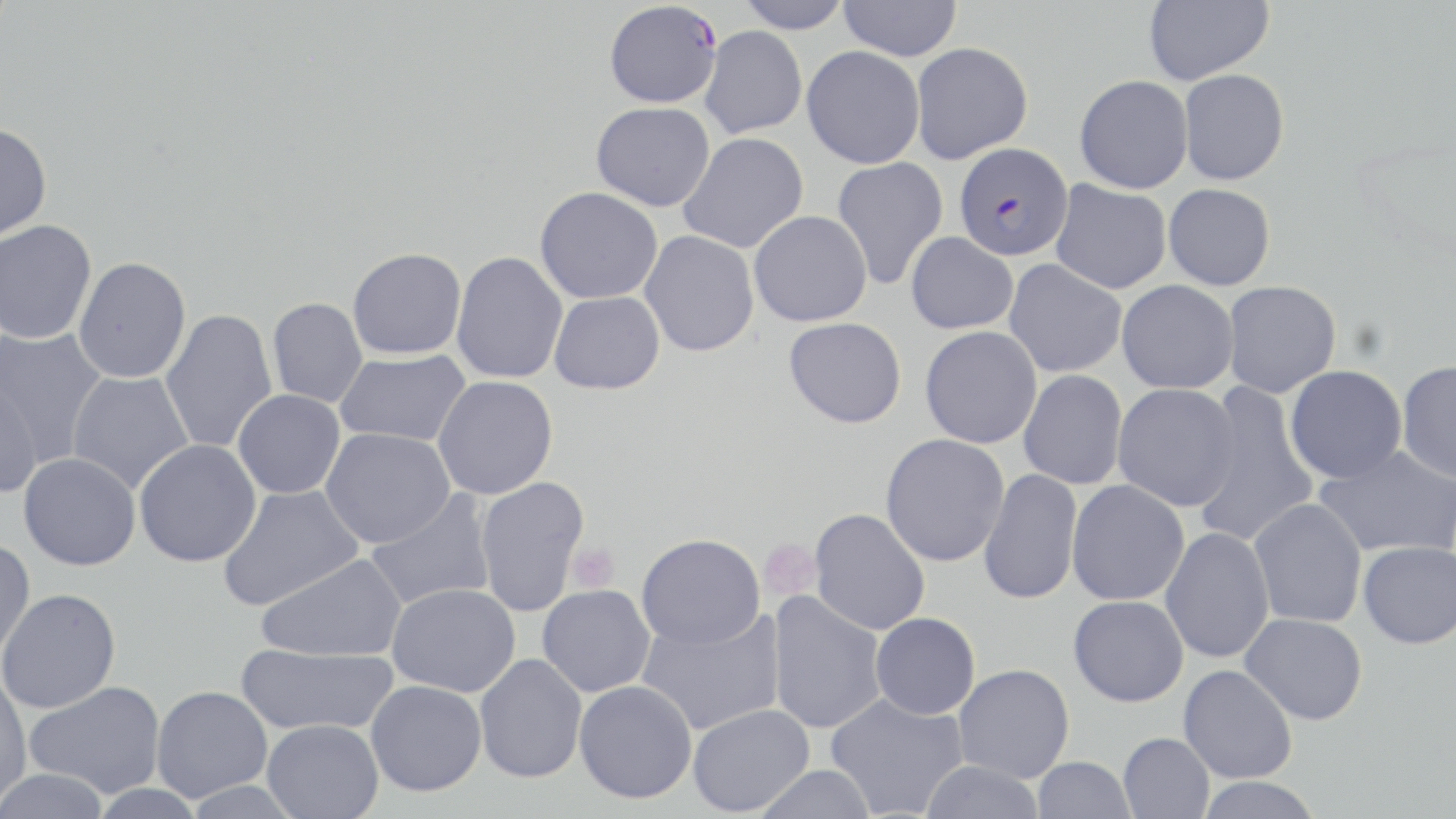

Summary:
  - Coordinate format: approximate bounding boxes as (x1, y1, x2, y2) in pixels
  - Plasmodium falciparum-infected red blood cell locations: (604, 1, 722, 108), (954, 142, 1074, 261)
  - Uninfected red blood cell locations: (734, 0, 853, 33), (838, 0, 962, 61), (1142, 0, 1273, 85), (700, 25, 807, 138), (910, 42, 1033, 164), (801, 46, 925, 168), (1178, 69, 1290, 186), (1074, 74, 1193, 194), (590, 101, 715, 212), (0, 122, 52, 242), (678, 132, 809, 254), (832, 158, 948, 290), (1051, 179, 1172, 294), (1163, 183, 1275, 291), (535, 187, 663, 304), (749, 210, 872, 327), (0, 219, 97, 345), (640, 230, 760, 357), (906, 232, 1018, 335), (347, 247, 466, 360), (451, 251, 568, 384), (73, 256, 192, 383), (1004, 259, 1127, 378), (1116, 280, 1239, 393), (1222, 280, 1341, 399), (549, 291, 665, 394), (267, 298, 367, 408), (159, 308, 278, 454), (784, 317, 907, 428), (920, 325, 1042, 449), (0, 326, 108, 469), (334, 350, 471, 447), (1397, 360, 1456, 484), (1284, 365, 1408, 484), (1018, 369, 1128, 490), (66, 370, 194, 494), (0, 375, 43, 499), (433, 375, 558, 499), (1191, 382, 1320, 549), (1112, 383, 1241, 511), (232, 389, 346, 499), (320, 427, 456, 548), (880, 433, 1010, 567), (134, 439, 262, 567), (1314, 445, 1456, 558), (19, 452, 141, 570), (979, 468, 1083, 605), (474, 476, 590, 618), (1066, 479, 1190, 606), (218, 484, 364, 611), (364, 490, 498, 612), (1249, 498, 1367, 628), (809, 508, 931, 635), (1160, 527, 1275, 664), (636, 533, 766, 649), (0, 538, 36, 662), (1358, 539, 1456, 649), (255, 553, 407, 662), (386, 582, 521, 698), (537, 584, 655, 697), (0, 588, 121, 713), (766, 591, 887, 734), (1068, 595, 1189, 707), (637, 608, 785, 736), (870, 612, 981, 720), (1240, 612, 1368, 725), (235, 643, 398, 736), (475, 654, 587, 783), (953, 664, 1075, 784), (1178, 664, 1298, 784), (0, 670, 33, 807), (24, 680, 166, 799), (366, 680, 486, 796), (574, 680, 698, 803), (151, 685, 272, 802), (825, 693, 969, 818), (688, 704, 814, 816), (262, 719, 383, 819), (1118, 732, 1215, 819), (1032, 756, 1136, 818), (918, 760, 1046, 819), (752, 764, 877, 819), (2, 768, 111, 819), (1193, 776, 1324, 819)
  - Platelet locations: (758, 538, 821, 602), (566, 541, 619, 593)
  - Slide-level diagnosis: Plasmodium falciparum
  - Preparation: thin blood film
  - Modality: light microscopy
  - Image size: 1456×819 pixels
  - Magnification: 1000x
  - Field of view: one of a larger specimen
  - Stain: May-Grünwald-Giemsa